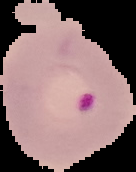
Image is 136×172 pixels. Cell region segmented out of the field of view; the surrounding area is masked to black. Malaria status: parasitized. From a thin blood film.